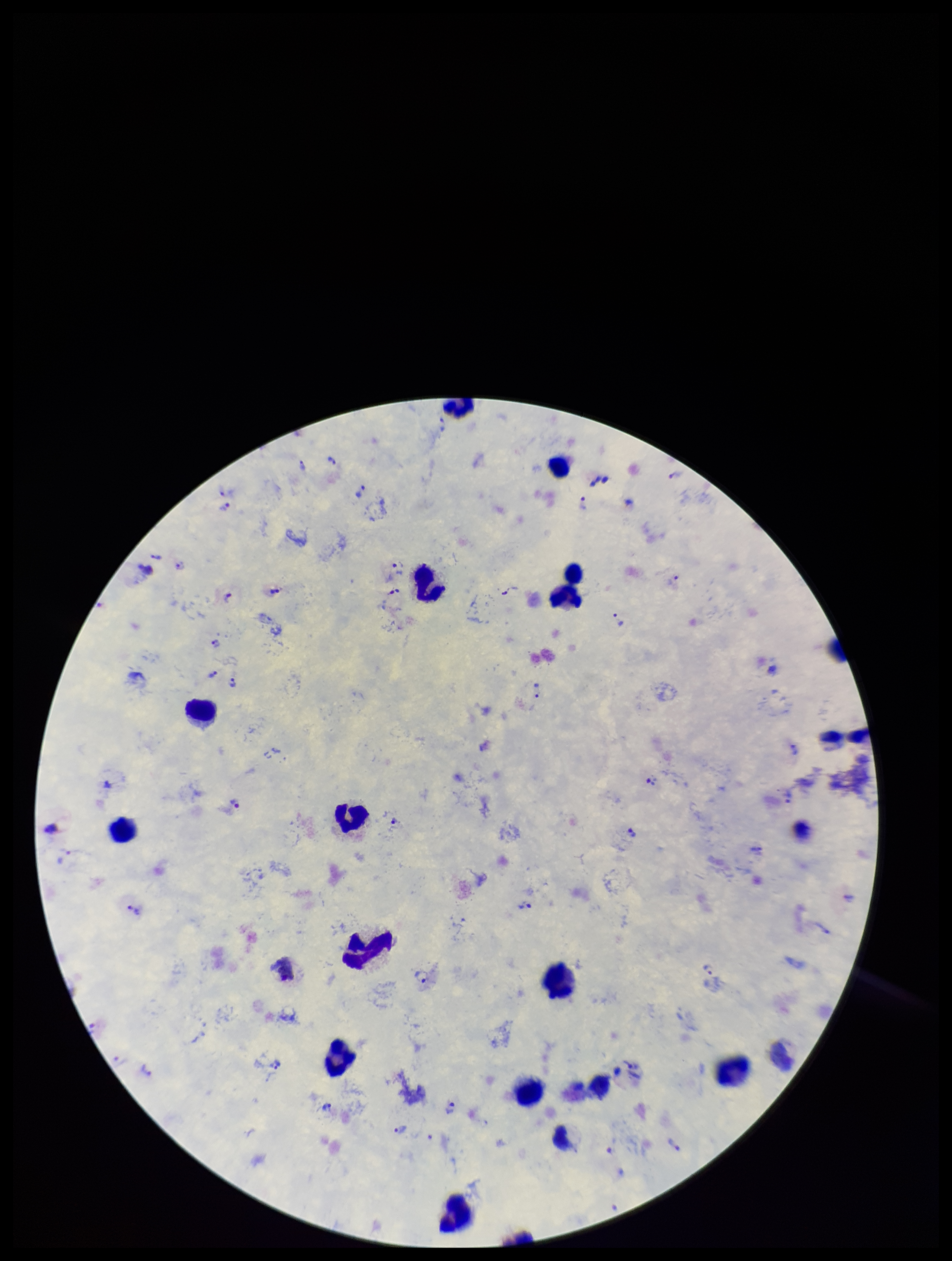
{
  "stain": "Giemsa",
  "preparation": "thick",
  "capture": "smartphone photograph through the microscope eyepiece",
  "image_size": "952×1261 pixels",
  "leukocyte_count": 15,
  "field_of_view": "single",
  "species_reported_for_this_patient": "Plasmodium vivax",
  "plasmodium_parasites": "detected",
  "parasite_count": 27,
  "patient_malaria_status": "positive"
}